Evaluate for Plasmodium parasites.
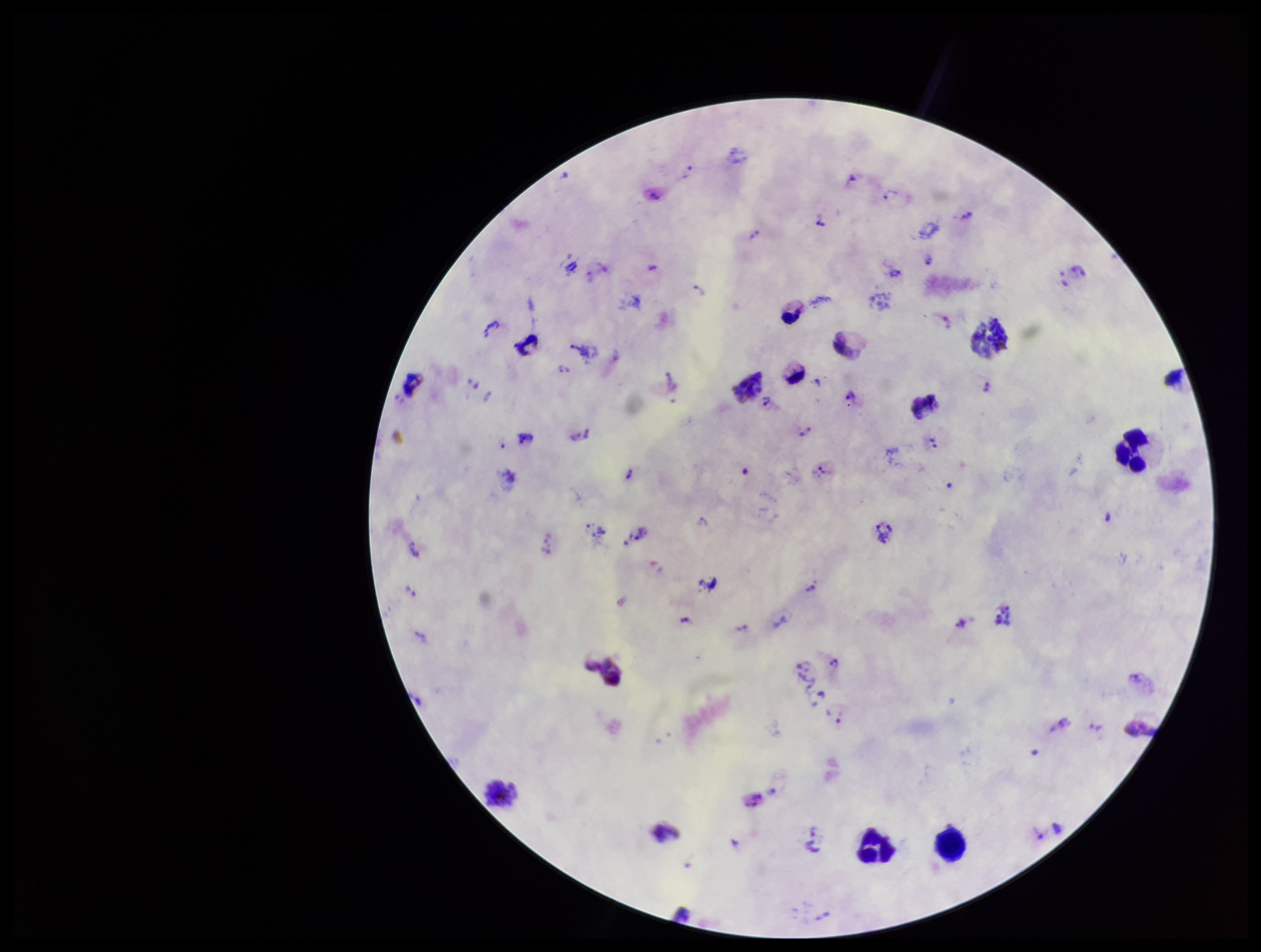

Identified.

Photographed through the microscope eyepiece with a smartphone camera. Giemsa stain. Leukocyte count: 15. Parasite count: 35. Species reported for this patient: Plasmodium vivax. Image is 1261×952 pixels. Patient malaria status: positive. Single field of view. Preparation: thick blood smear.